Point out each leukocyte.
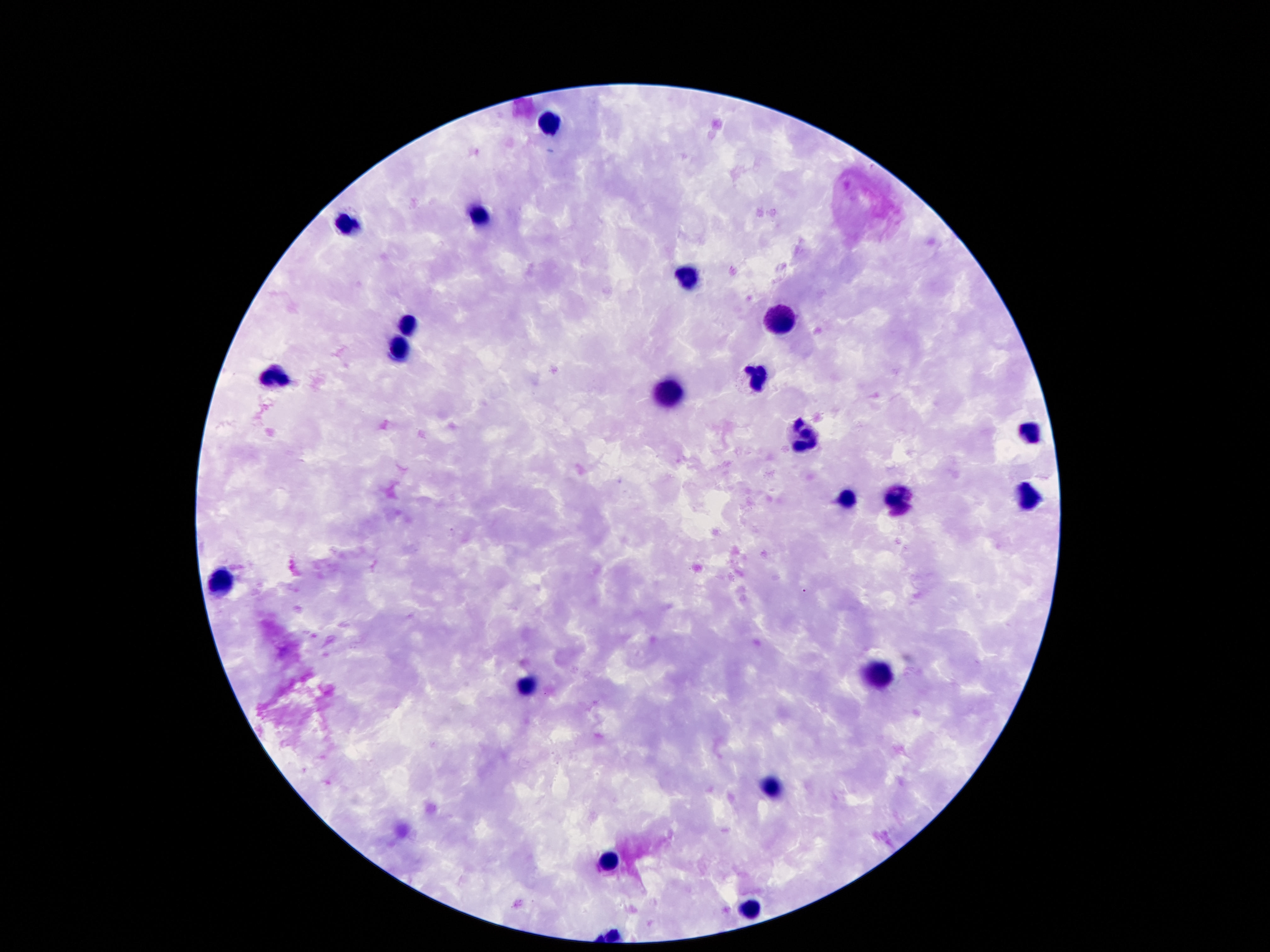

Approximate centers as [x, y] in pixels.
Leukocytes: [546, 124], [477, 217], [346, 228], [685, 276], [781, 321], [409, 328], [399, 349], [273, 377], [754, 378], [668, 395], [1033, 436], [804, 437], [848, 498], [1027, 500], [896, 502], [223, 584], [882, 672], [527, 690], [771, 786], [609, 859], [752, 912].

One field from this slide. Patient malaria status: uninfected. Image is 1270×952 pixels. Thick blood film. Smartphone photograph taken through the microscope eyepiece. 100x magnification. Giemsa-stained preparation.